Give the position of every malaria parasite, noting whether each is a trophozoite, schizont, or gametocyte.
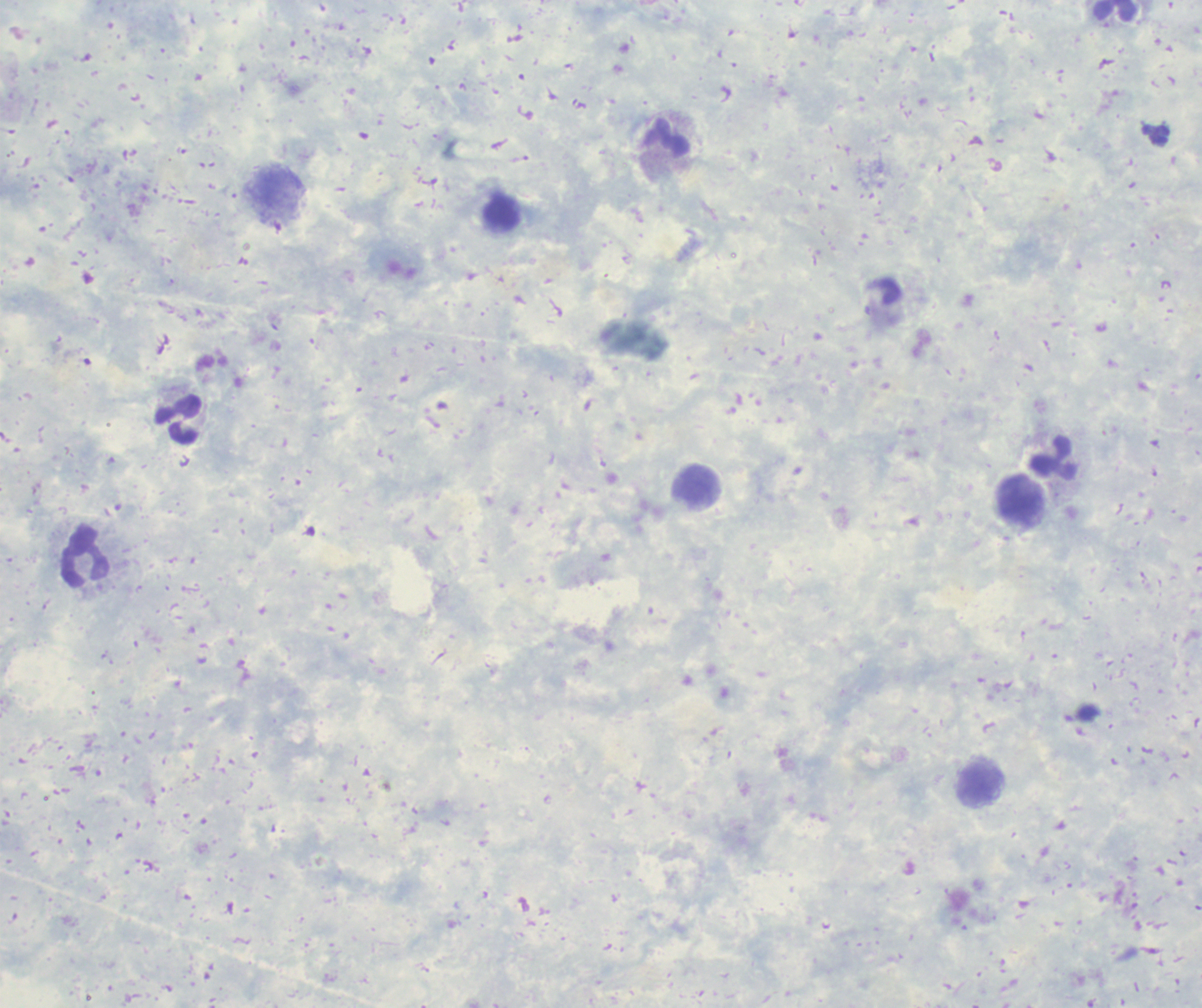
No malaria parasites seen.

Approximate centers as (x, y) in pixels.
Summary:
  - Leukocyte locations: (1115, 11), (667, 138), (177, 419), (1054, 458), (694, 485), (1019, 501), (85, 556), (981, 782)
  - Background quality: poor
  - Preparation: thick smear of blood
  - Context: previously used in an actual diagnosis
  - Field of view: single
  - Image size: 1202×1008 pixels
  - Stain: Romanowsky
  - Magnification: 100x